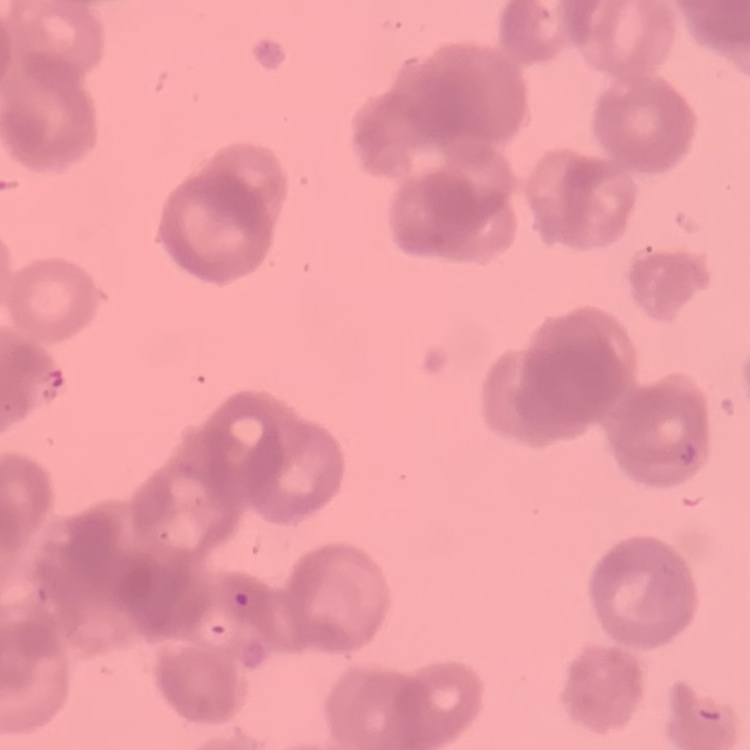
The erythrocytes exhibit rouleaux formation. Thin blood film. Stained with either Field's or Giemsa. Square crop of a larger photomicrograph.